Describe the morphology of the red blood cells.
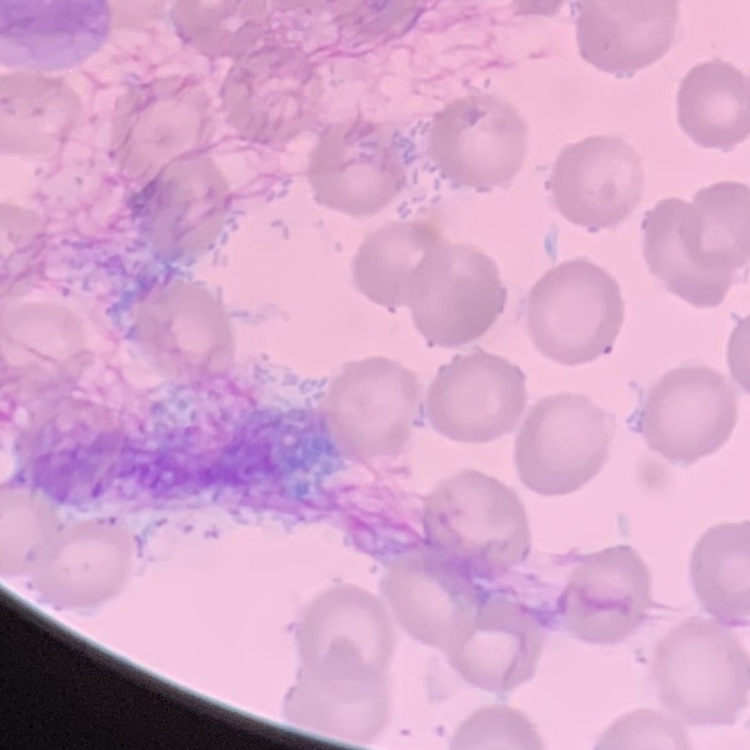
They show no rouleaux formation.

Summary:
  - Preparation: thin peripheral smear
  - Stain: Field's or Giemsa
  - Image type: one tile cut from a larger photomicrograph